Describe the morphology of the red blood cells.
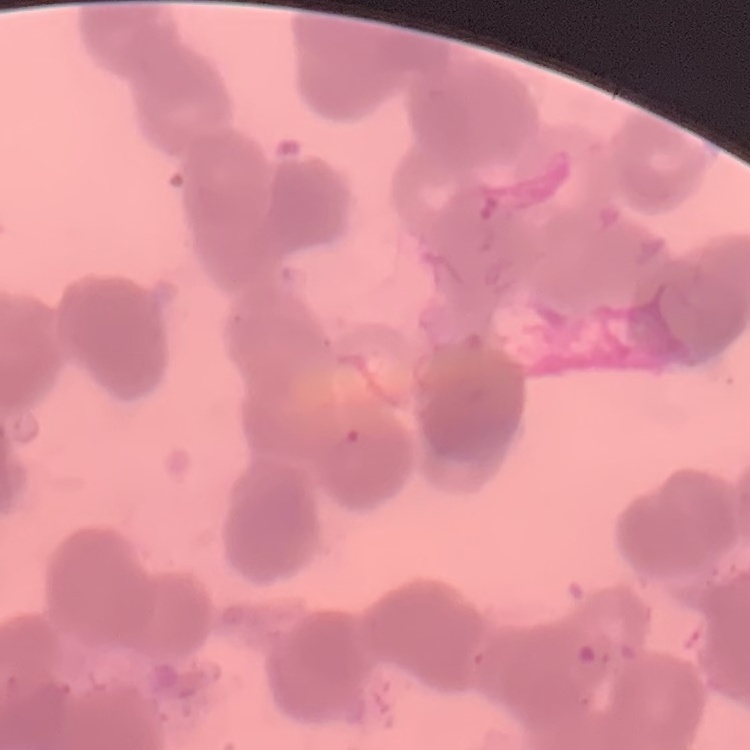
Rouleaux formation.

Summary:
  - Image type: square crop of a larger photomicrograph
  - Stain: Field's or Giemsa
  - Preparation: thin blood film